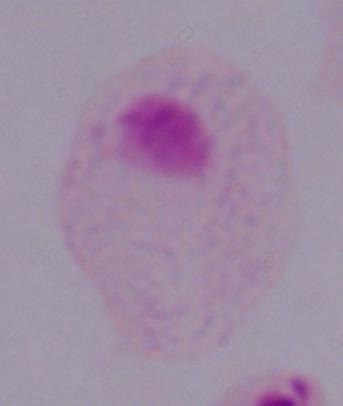 Photomicrograph. Captured at 1000x magnification. A trichomonad is shown.